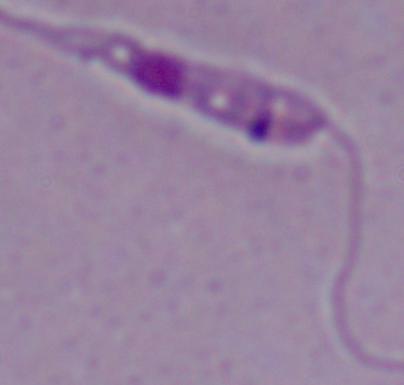
Summary:
  - Magnification: 1000x
  - Modality: photomicrograph
  - Identification: Leishmania